Identify the cell.
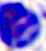

A leukocyte.

magnification = 400x
modality = photomicrograph